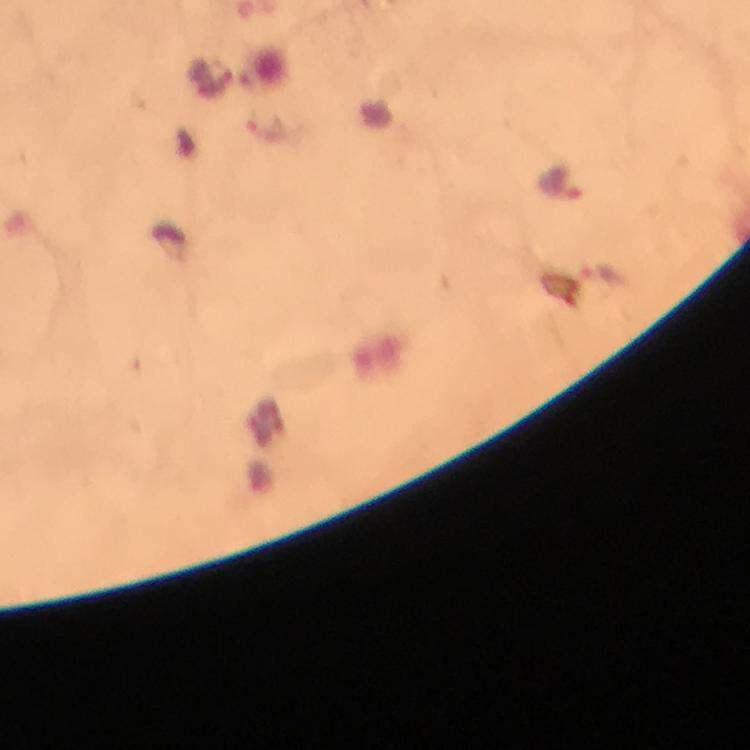
Approximate centers as [x, y] in pixels.
Summary:
  - Plasmodium parasite locations: [562, 182]
  - Stain: Giemsa
  - Immersion oil: applied
  - Image size: 750×750 pixels
  - Context: from a diagnostic examination for malaria
  - Cropped from: a single field of view
  - Capture: smartphone photograph through a microscope
  - Magnification: 100x
  - Preparation: thick blood smear